Locate every Plasmodium falciparum-infected red blood cell.
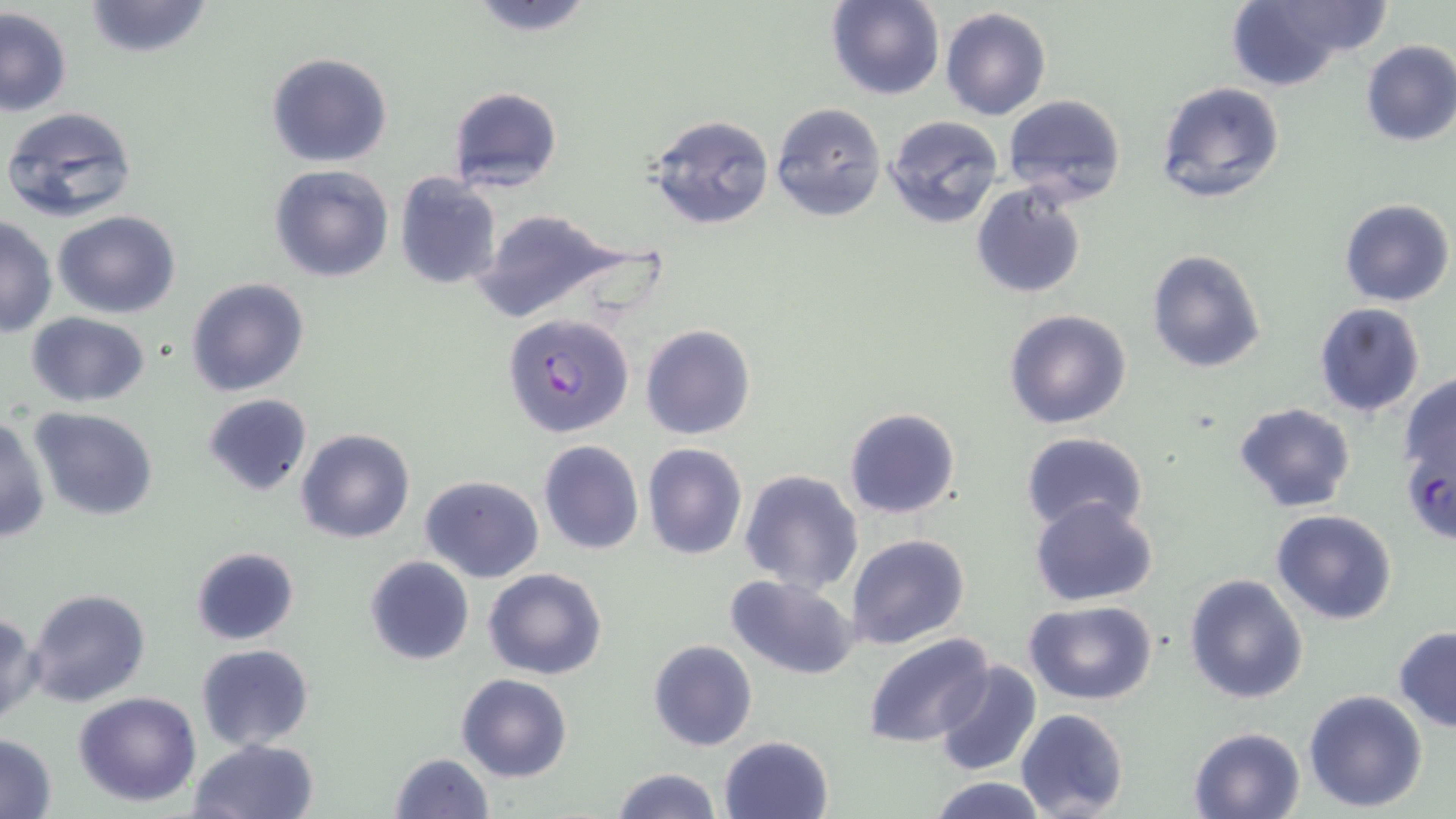
Approximate bounding boxes as [x1, y1, x2, y2] in pixels.
Plasmodium falciparum-infected red blood cells: [503, 313, 635, 439].

Uninfected red blood cell locations: [82, 0, 213, 57], [825, 0, 944, 101], [1222, 0, 1388, 92], [461, 2, 599, 35], [0, 8, 73, 117], [939, 8, 1051, 120], [1359, 39, 1456, 147], [266, 53, 393, 168], [1154, 81, 1288, 206], [448, 86, 562, 194], [1002, 94, 1128, 205], [770, 102, 887, 222], [2, 104, 139, 223], [648, 114, 775, 230], [884, 115, 1004, 229], [268, 163, 396, 283], [394, 171, 503, 291], [969, 184, 1089, 299], [1338, 197, 1454, 308], [468, 208, 654, 325], [53, 210, 182, 318], [1, 215, 56, 337], [1146, 248, 1267, 374], [186, 278, 310, 398], [1312, 302, 1427, 418], [1003, 308, 1132, 429], [26, 311, 149, 407], [639, 323, 757, 441], [1395, 372, 1456, 536], [202, 393, 313, 496], [1231, 402, 1358, 514], [30, 407, 158, 521], [843, 407, 962, 519], [0, 414, 51, 544], [296, 428, 416, 545], [1019, 433, 1149, 532], [538, 440, 644, 555], [642, 443, 748, 561], [738, 468, 864, 594], [419, 474, 544, 583], [1030, 495, 1160, 606], [1270, 509, 1399, 626], [844, 534, 969, 651], [190, 546, 300, 647], [364, 555, 474, 666], [482, 567, 608, 680], [1183, 573, 1309, 704], [724, 575, 859, 678], [26, 588, 152, 707], [1023, 601, 1159, 706], [0, 612, 41, 727], [1394, 627, 1456, 733], [864, 631, 995, 748], [648, 639, 757, 751], [194, 644, 315, 750], [933, 660, 1041, 778], [456, 673, 572, 783], [1303, 688, 1430, 812], [72, 692, 203, 807], [1015, 708, 1129, 819], [1187, 725, 1309, 818], [1, 734, 58, 817], [718, 735, 835, 819], [188, 738, 321, 819], [388, 751, 495, 819], [611, 767, 721, 819], [925, 777, 1052, 818]. Slide-level diagnosis: Plasmodium falciparum. One field of a larger specimen. Image is 1456×819 pixels. May-Grünwald-Giemsa-stained preparation. Light microscopy. Captured at 1000x magnification. Thin blood film.